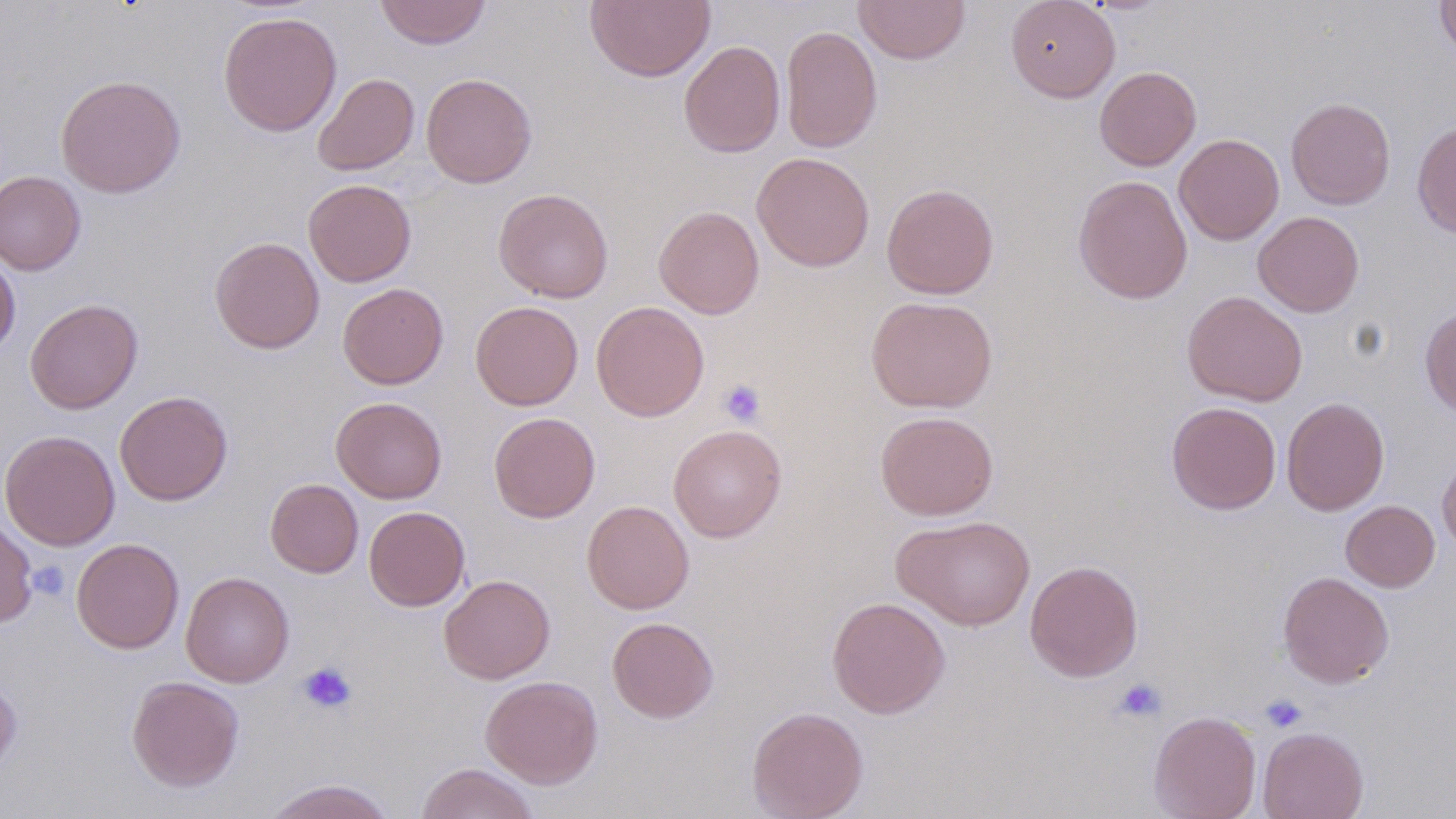
Summary:
  - Coordinate format: approximate bounding boxes as named x1/y1/x2/y2 corners in pixels
  - Platelet locations: (x1=718, y1=378, x2=766, y2=428), (x1=28, y1=560, x2=70, y2=601), (x1=297, y1=661, x2=357, y2=714), (x1=1112, y1=677, x2=1167, y2=723), (x1=1259, y1=694, x2=1308, y2=733)
  - Uninfected red blood cell locations: (x1=374, y1=0, x2=491, y2=49), (x1=584, y1=0, x2=716, y2=83), (x1=853, y1=0, x2=970, y2=65), (x1=1005, y1=0, x2=1120, y2=102), (x1=1435, y1=0, x2=1456, y2=63), (x1=218, y1=11, x2=343, y2=137), (x1=780, y1=25, x2=882, y2=153), (x1=679, y1=41, x2=785, y2=158), (x1=1094, y1=66, x2=1201, y2=170), (x1=421, y1=72, x2=537, y2=188), (x1=313, y1=73, x2=419, y2=175), (x1=56, y1=74, x2=186, y2=198), (x1=1286, y1=97, x2=1396, y2=210), (x1=1412, y1=120, x2=1456, y2=238), (x1=1173, y1=133, x2=1284, y2=245), (x1=751, y1=152, x2=875, y2=272), (x1=0, y1=171, x2=86, y2=275), (x1=1073, y1=175, x2=1193, y2=304), (x1=303, y1=178, x2=416, y2=287), (x1=882, y1=183, x2=999, y2=299), (x1=493, y1=188, x2=613, y2=303), (x1=653, y1=205, x2=764, y2=319), (x1=1253, y1=211, x2=1365, y2=317), (x1=210, y1=236, x2=325, y2=353), (x1=0, y1=255, x2=20, y2=358), (x1=338, y1=283, x2=448, y2=389), (x1=1182, y1=290, x2=1307, y2=407), (x1=866, y1=295, x2=998, y2=413), (x1=24, y1=298, x2=143, y2=414), (x1=471, y1=301, x2=584, y2=410), (x1=591, y1=301, x2=709, y2=421), (x1=1419, y1=307, x2=1456, y2=418), (x1=114, y1=390, x2=233, y2=506), (x1=331, y1=396, x2=447, y2=503), (x1=1281, y1=397, x2=1390, y2=516), (x1=1166, y1=402, x2=1281, y2=514), (x1=875, y1=411, x2=998, y2=520), (x1=488, y1=412, x2=600, y2=523), (x1=668, y1=424, x2=787, y2=542), (x1=1, y1=430, x2=120, y2=551), (x1=1437, y1=449, x2=1456, y2=555), (x1=265, y1=478, x2=363, y2=577), (x1=581, y1=499, x2=694, y2=614), (x1=1341, y1=500, x2=1440, y2=592), (x1=364, y1=506, x2=470, y2=611), (x1=0, y1=515, x2=37, y2=626), (x1=892, y1=515, x2=1035, y2=631), (x1=71, y1=538, x2=184, y2=653), (x1=1024, y1=559, x2=1143, y2=681), (x1=181, y1=571, x2=294, y2=687), (x1=1277, y1=571, x2=1395, y2=688), (x1=439, y1=574, x2=555, y2=684), (x1=826, y1=596, x2=950, y2=718), (x1=607, y1=617, x2=719, y2=723), (x1=0, y1=673, x2=22, y2=775), (x1=126, y1=675, x2=245, y2=792), (x1=480, y1=675, x2=603, y2=788), (x1=747, y1=706, x2=868, y2=819), (x1=1149, y1=710, x2=1262, y2=819), (x1=1257, y1=726, x2=1369, y2=819), (x1=415, y1=763, x2=540, y2=819), (x1=262, y1=778, x2=397, y2=819)
  - Slide-level diagnosis: no evidence of blood parasites
  - Preparation: thin blood smear
  - Stain: May-Grünwald-Giemsa
  - Modality: optical microscopy
  - Field of view: one of a larger specimen
  - Image size: 1456×819 pixels
  - Magnification: 1000x